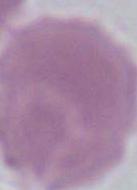
{
  "magnification": "1000x",
  "modality": "photomicrograph",
  "identification": "erythrocyte"
}